Assess this cell for malaria.
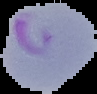
It is parasitized.

From a thin blood film. Segmented cell region on a black background. Image is 97×94 pixels.